Assess this cell for malaria.
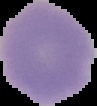

It is parasitized.

Summary:
  - Image size: 97×106 pixels
  - Image type: segmented cell region with the area outside set to black
  - Preparation: thin blood smear